Report the malaria status of this cell.
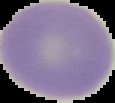
It is uninfected.

preparation = thin blood film
image size = 115×103 pixels
image type = segmented cell region with the area outside set to black